Locate every Plasmodium parasite.
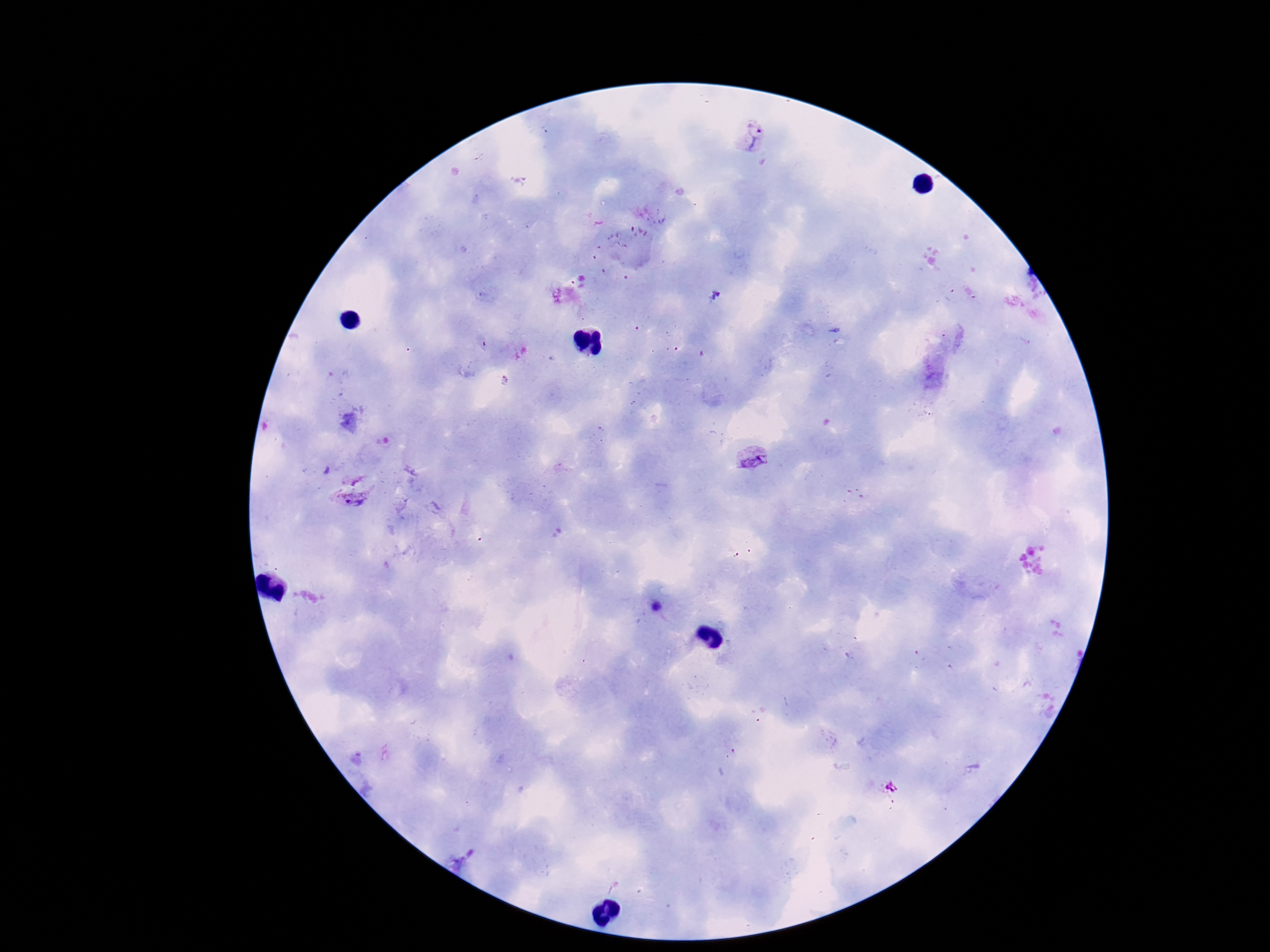

Approximate object centers, in pixels from the top-left corner.
Plasmodium parasites: (x=752, y=137), (x=752, y=456), (x=355, y=497), (x=657, y=607).

Summary:
  - Capture: smartphone camera through the microscope eyepiece
  - Image size: 1270×952 pixels
  - Patient malaria status: infected
  - Magnification: 100x
  - Preparation: thick blood smear
  - Stain: Giemsa
  - Field of view: single